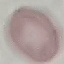
malaria status = uninfected
capture = smartphone through the microscope eyepiece
stain = Giemsa
image type = cell patch, automatically extracted from a larger field of view and resized to 64 × 64 pixels
preparation = thin blood smear